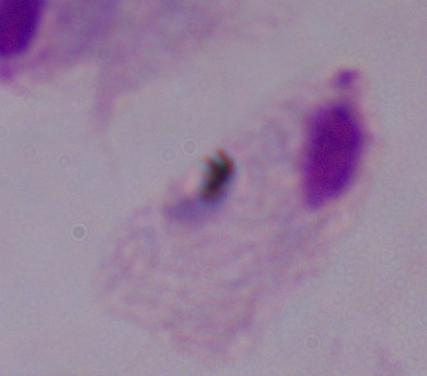
A trichomonad is shown. Micrograph. 1000x magnification.